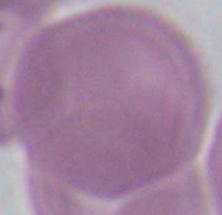

Photomicrograph. An erythrocyte is shown. Captured at 1000x magnification.